Assess the morphology of the erythrocytes.
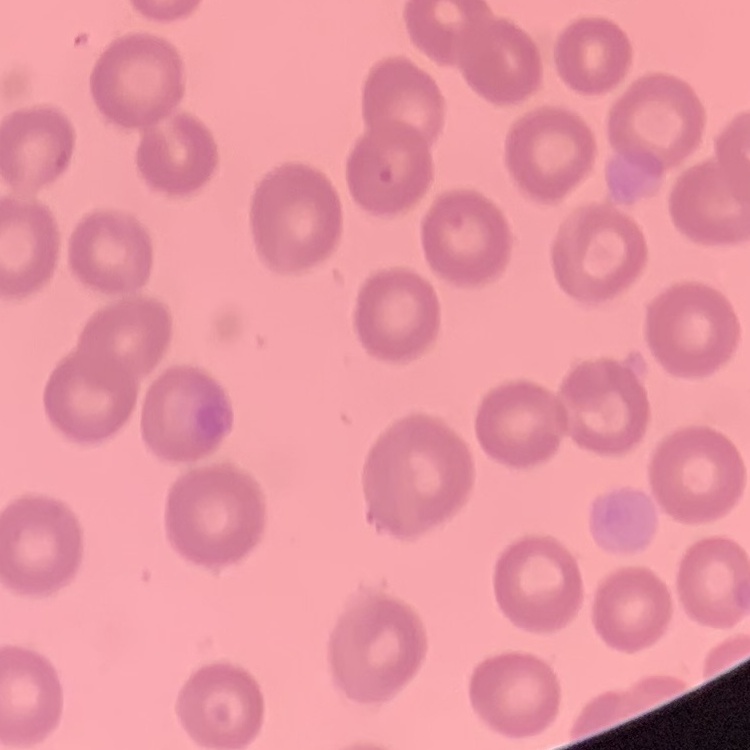

No rouleaux formation.

Summary:
  - Image type: one tile cut from a larger photomicrograph
  - Preparation: thin blood smear
  - Stain: Field's or Giemsa